Locate every Plasmodium falciparum-infected red blood cell.
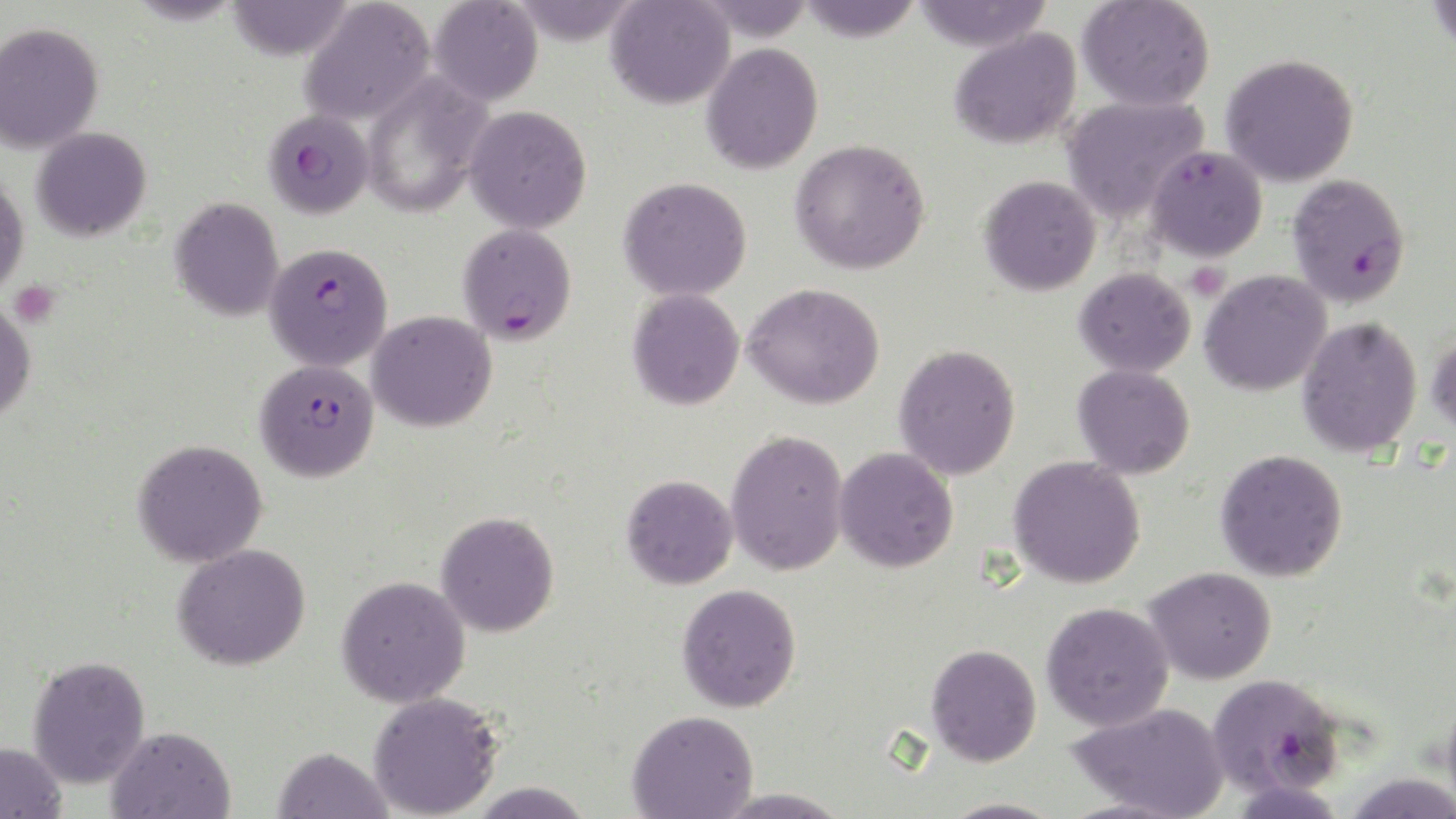
Approximate bounding boxes as (x1,y1)-(x2,y2) corner pairs in pixels.
Plasmodium falciparum-infected red blood cells: (262,108)-(374,219), (1286,173)-(1412,308), (457,223)-(577,345), (264,242)-(393,371), (255,359)-(380,482), (1206,672)-(1346,798).

Summary:
  - Platelet locations: (1185,261)-(1229,301), (10,280)-(60,327)
  - Uninfected red blood cell locations: (225,0)-(353,61), (299,0)-(436,127), (429,0)-(543,105), (508,0)-(642,44), (691,0)-(816,41), (795,0)-(924,42), (912,0)-(1053,52), (1077,0)-(1215,112), (1424,0)-(1456,54), (605,1)-(734,109), (0,22)-(104,153), (949,28)-(1081,149), (701,42)-(824,175), (1221,53)-(1360,187), (361,72)-(494,218), (1061,94)-(1209,223), (464,105)-(592,234), (31,127)-(152,241), (790,138)-(931,275), (1145,144)-(1268,262), (0,172)-(28,299), (978,175)-(1101,296), (618,176)-(753,301), (170,196)-(284,321), (1074,266)-(1196,377), (1200,269)-(1332,397), (743,282)-(885,410), (628,288)-(745,410), (0,298)-(37,424), (368,311)-(497,432), (1297,315)-(1423,458), (1426,329)-(1456,441), (894,343)-(1021,480), (1073,363)-(1196,479), (726,429)-(849,576), (132,439)-(268,567), (834,447)-(958,572), (1215,449)-(1348,581), (1009,456)-(1146,589), (621,474)-(738,590), (436,511)-(560,637), (173,543)-(311,671), (1143,566)-(1277,685), (337,575)-(471,707), (677,583)-(801,713), (1041,601)-(1174,731), (925,643)-(1042,766), (27,654)-(150,789), (1441,686)-(1456,819), (368,692)-(503,818), (1068,701)-(1230,819), (627,709)-(758,819), (106,725)-(236,818), (0,742)-(67,819), (273,746)-(392,819), (467,781)-(595,818), (712,787)-(851,818), (939,797)-(1065,818)
  - Slide-level diagnosis: Plasmodium falciparum
  - Preparation: thin blood film
  - Modality: optical microscopy
  - Magnification: 1000x
  - Stain: May-Grünwald-Giemsa
  - Image size: 1456×819 pixels
  - Field of view: single